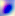

Summary:
  - Magnification: 400x
  - Identification: Toxoplasma gondii
  - Modality: micrograph